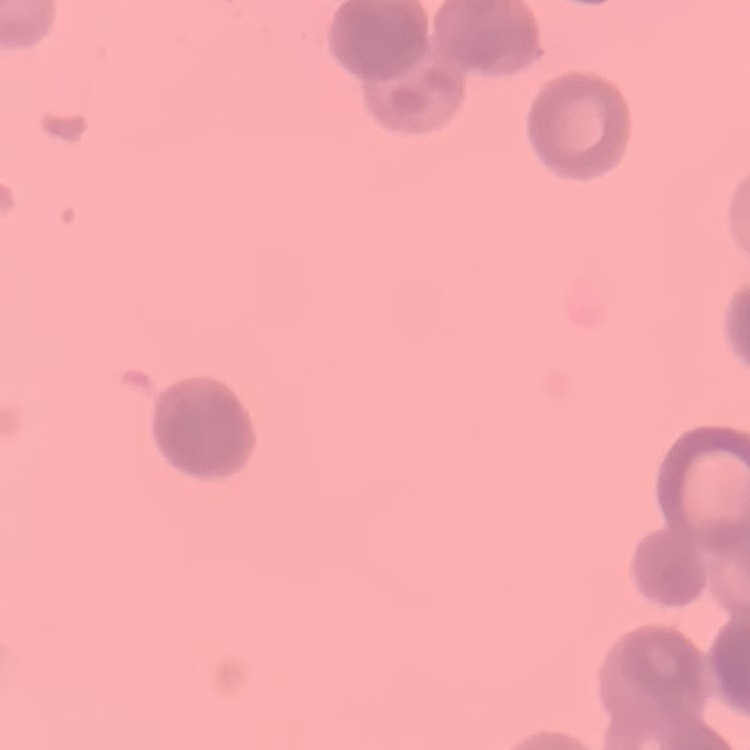
{
  "erythrocyte_morphology": "rouleaux formation",
  "stain": "Field's or Giemsa",
  "preparation": "thin blood film",
  "image_type": "one tile cut from a larger photomicrograph"
}